Identify the parasite.
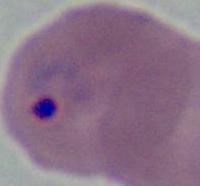
This is Plasmodium.

Captured at either 400x or 1000x magnification. Photomicrograph.